Locate and identify every blood parasite.
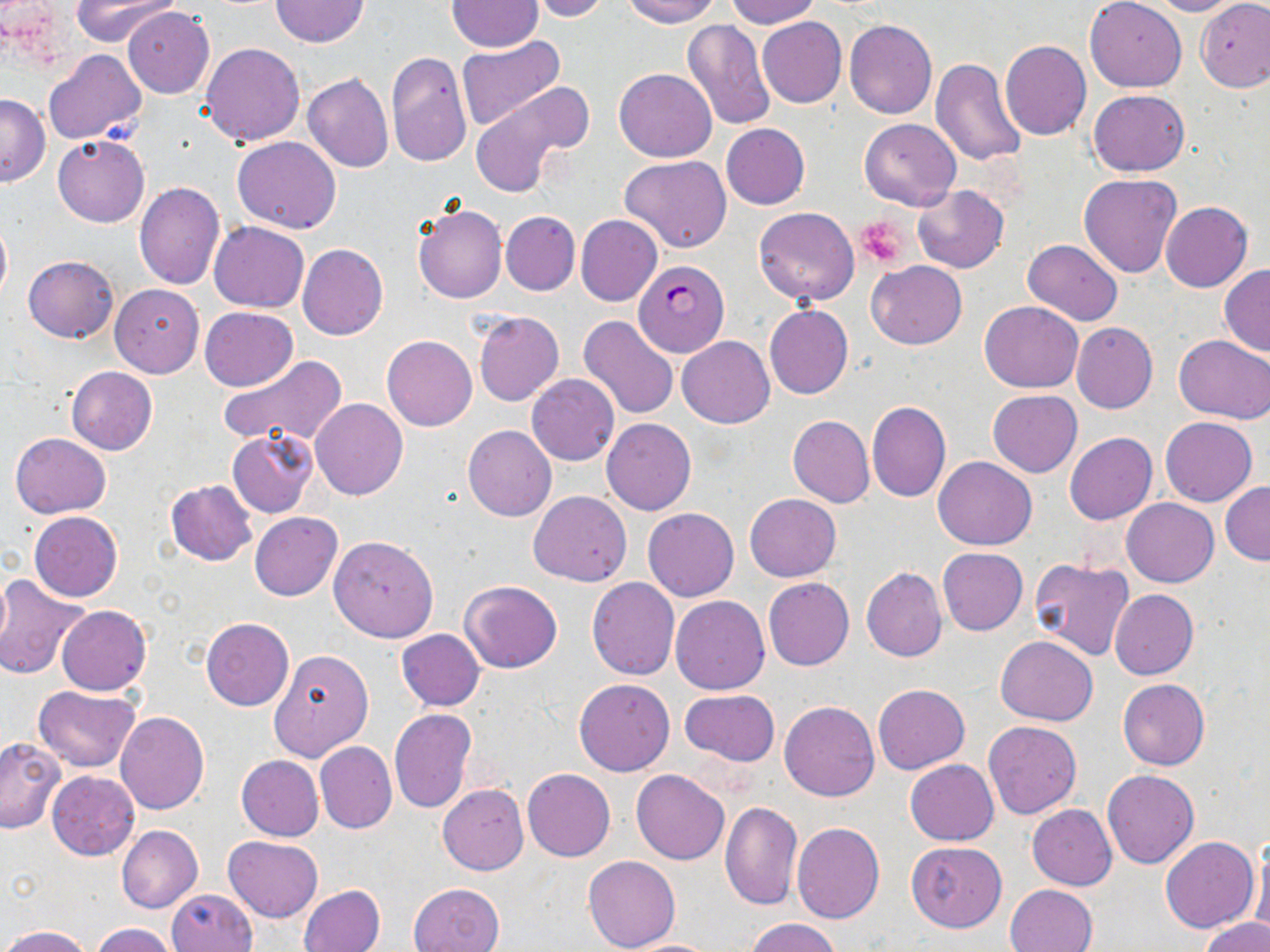

Approximate bounding boxes as [x1, y1, x2, y2] in pixels.
Plasmodium falciparum-infected red blood cells: [635, 260, 729, 358].
No Plasmodium ovale, Plasmodium malariae, Plasmodium vivax, Babesia divergens, or Trypanosoma brucei observed.

slide-level diagnosis = Plasmodium falciparum
magnification = 1000x
modality = light microscopy
uninfected red blood cell locations = approximate bounding boxes as [x1, y1, x2, y2] in pixels: [72, 0, 180, 48], [270, 0, 368, 47], [524, 0, 611, 21], [620, 0, 723, 27], [724, 0, 820, 27], [1084, 0, 1187, 92], [1150, 0, 1242, 17], [1195, 0, 1270, 92], [446, 2, 543, 52], [123, 6, 214, 98], [757, 16, 846, 108], [682, 20, 776, 130], [845, 20, 937, 119], [459, 37, 566, 131], [1000, 41, 1092, 141], [201, 42, 305, 147], [43, 49, 146, 145], [385, 52, 471, 167], [930, 58, 1029, 168], [614, 67, 717, 162], [302, 74, 393, 173], [471, 88, 584, 196], [1087, 88, 1190, 176], [1, 95, 50, 185], [859, 117, 961, 210], [720, 123, 810, 209], [53, 134, 149, 227], [233, 136, 341, 234], [620, 155, 732, 252], [1078, 174, 1182, 278], [133, 182, 224, 288], [912, 184, 1008, 273], [1161, 202, 1253, 292], [413, 204, 507, 304], [754, 207, 859, 306], [501, 211, 579, 294], [575, 214, 664, 306], [0, 217, 11, 305], [209, 222, 308, 311], [1022, 238, 1122, 325], [297, 243, 389, 340], [22, 255, 119, 342], [867, 261, 967, 350], [1219, 265, 1270, 356], [110, 283, 203, 377], [979, 301, 1083, 393], [764, 304, 853, 399], [199, 307, 298, 390], [474, 312, 564, 406], [578, 316, 680, 422], [1071, 322, 1158, 413], [382, 334, 477, 430], [1174, 335, 1270, 424], [677, 336, 775, 429], [217, 354, 348, 452], [66, 366, 158, 455], [527, 373, 619, 465], [988, 389, 1082, 477], [310, 398, 408, 501], [866, 401, 952, 501], [787, 415, 874, 508], [602, 417, 697, 515], [1161, 417, 1257, 506], [463, 425, 557, 520], [227, 430, 317, 518], [10, 432, 111, 518], [1064, 432, 1157, 525], [934, 456, 1036, 550], [165, 479, 257, 567], [1220, 482, 1270, 565], [528, 491, 632, 585], [744, 493, 841, 581], [1122, 497, 1219, 588], [643, 507, 739, 602], [29, 511, 122, 602], [250, 512, 343, 600], [329, 535, 438, 642], [936, 548, 1028, 635], [1028, 558, 1133, 662], [861, 568, 946, 662], [0, 574, 91, 680], [586, 577, 679, 680], [763, 577, 854, 671], [459, 581, 563, 673], [1109, 588, 1198, 679], [671, 595, 769, 694], [56, 605, 151, 695], [201, 617, 294, 711], [396, 629, 485, 710], [996, 635, 1098, 725], [268, 649, 373, 762], [574, 678, 675, 776], [1117, 679, 1210, 770], [873, 684, 969, 774], [32, 686, 140, 770], [679, 689, 779, 765], [780, 700, 879, 801], [389, 708, 478, 815], [116, 712, 209, 815], [982, 721, 1083, 819], [0, 738, 64, 833], [316, 742, 396, 834], [236, 756, 324, 840], [905, 759, 998, 846], [522, 768, 616, 861], [632, 770, 729, 865], [1103, 770, 1198, 869], [46, 771, 139, 860], [437, 784, 528, 875], [719, 800, 803, 911], [1027, 805, 1117, 890], [1017, 808, 1107, 952], [791, 822, 885, 924], [116, 825, 202, 913], [223, 836, 324, 922], [1161, 836, 1259, 933], [907, 841, 1006, 932], [1249, 841, 1270, 940], [582, 855, 681, 951], [408, 882, 505, 952], [1005, 884, 1096, 952], [299, 885, 384, 952], [166, 888, 256, 952], [1200, 917, 1269, 952], [747, 918, 840, 952], [90, 923, 178, 952], [3, 925, 92, 952], [617, 938, 722, 952]
image size = 1270×952 pixels
stain = May-Grünwald-Giemsa
preparation = thin blood smear
field of view = single
platelet locations = approximate bounding boxes as [x1, y1, x2, y2] in pixels: [859, 219, 910, 267]